Point out each Plasmodium parasite and each leukocyte.
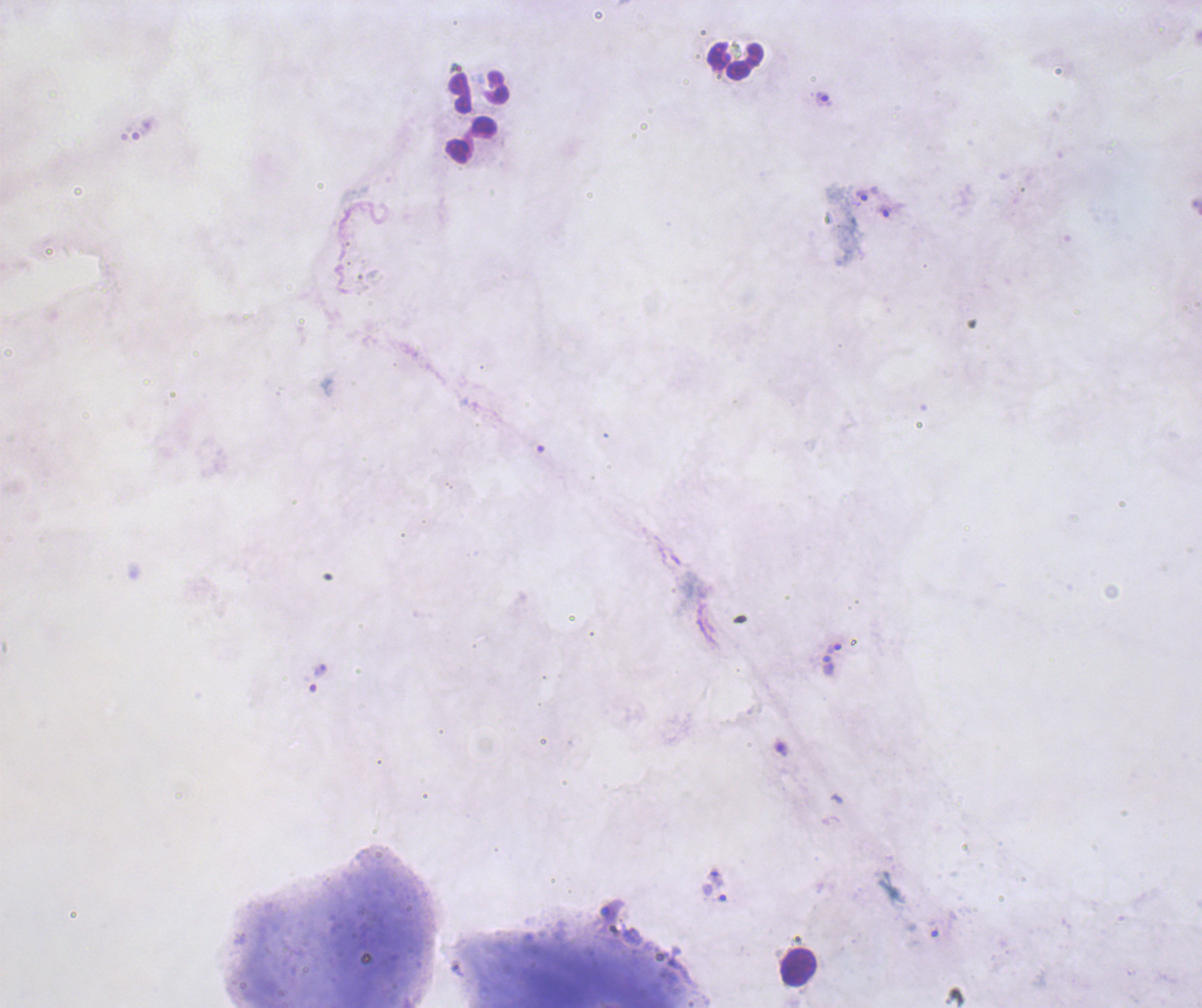
Approximate centers as (x, y) in pixels.
Trophozoites: (824, 99), (862, 195), (884, 211), (834, 648), (828, 666), (716, 877), (714, 893).
No schizont or gametocyte forms observed.
Leukocytes: (735, 60), (479, 92), (471, 139), (798, 967).

Summary:
  - Preparation: thick blood smear
  - Background quality: poor
  - Coloration quality: bad
  - Context: previously used in an actual diagnosis
  - Image size: 1202×1008 pixels
  - Stain: Romanowsky
  - Field of view: single
  - Magnification: 100x